Report the malaria status of this cell.
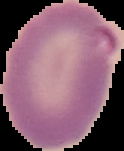

Parasitized.

Summary:
  - Preparation: thin blood film
  - Image type: cell region segmented out of the field of view; surrounding area masked to black
  - Image size: 124×151 pixels